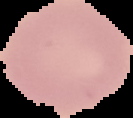

From a thin blood film. Image is 133×118 pixels. Malaria status: uninfected. Cell region segmented out of the field of view; the surrounding area is masked to black.